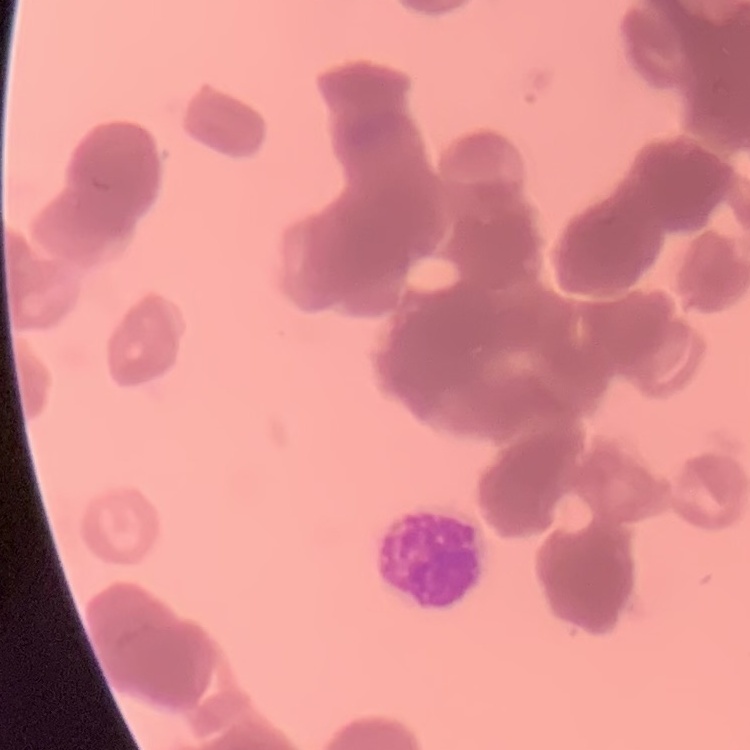

erythrocyte morphology = rouleaux formation
image type = square crop of a larger photomicrograph
stain = Field's or Giemsa
preparation = thin blood film